Classify this cell by malaria status.
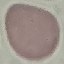
It is uninfected.

Giemsa stain. Thin blood film. Photographed with a smartphone camera at the microscope eyepiece. Automatically extracted cell patch, resized to 64 × 64 pixels.